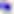 Photomicrograph. Toxoplasma gondii is shown. 400x magnification.